Give the preparation type.
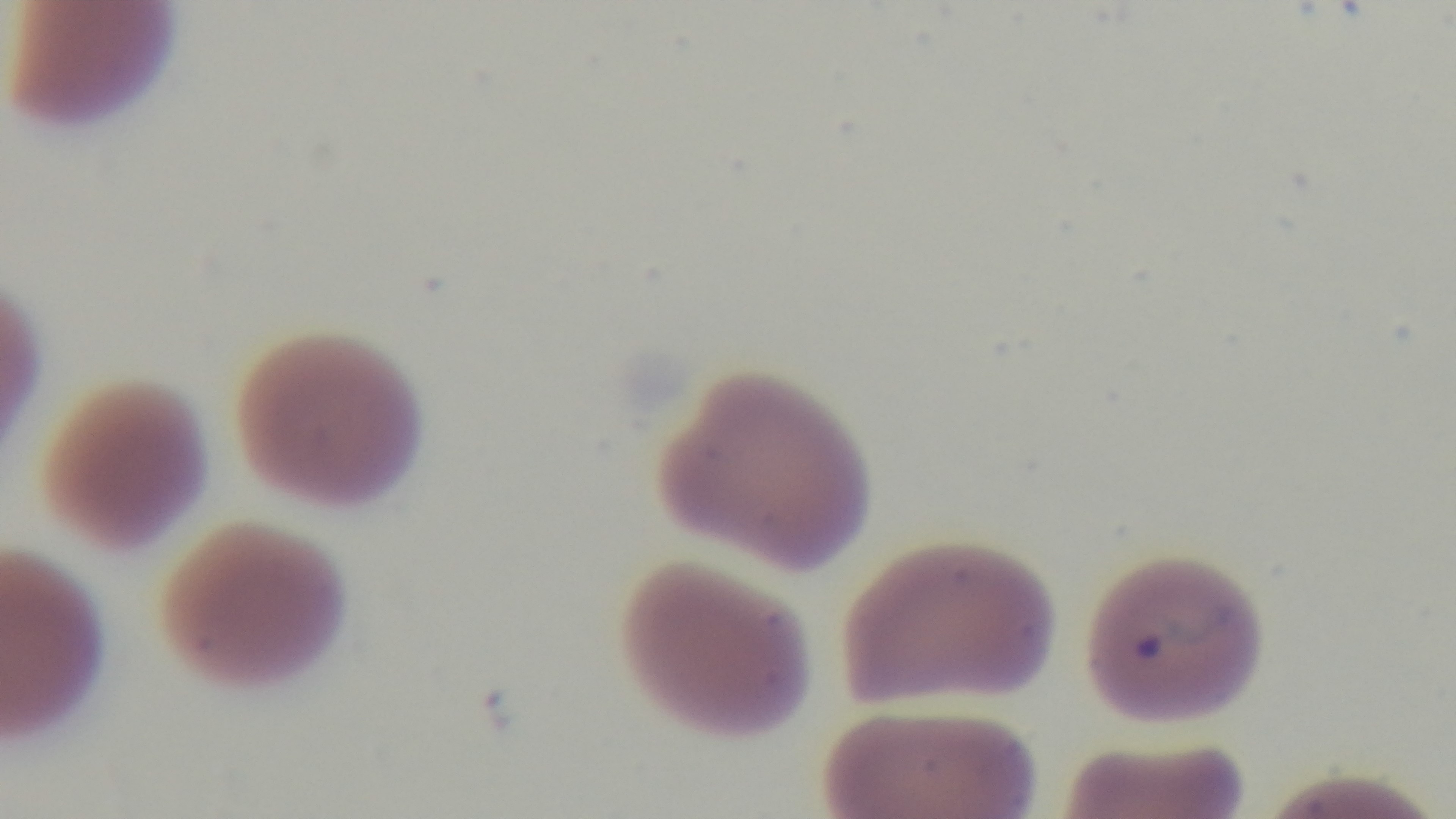
A thin smear.

Malaria status: positive. Mounted 4K digital camera. One field from the slide. Giemsa stain. 100x oil-immersion objective. Photomicrograph.